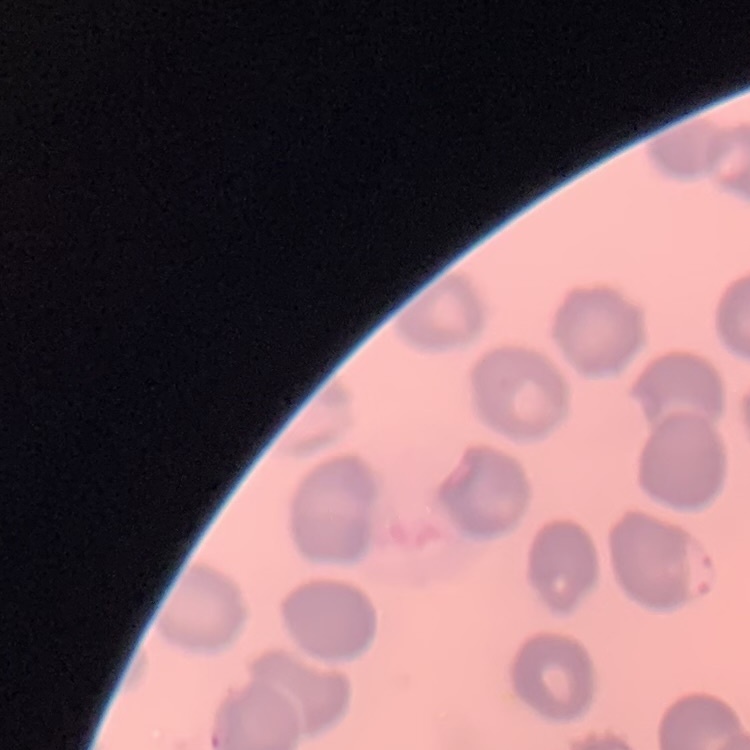
The red blood cells exhibit no rouleaux formation. Thin blood film. One tile cut from a larger photomicrograph. Field's or Giemsa stain.